Identify the parasite.
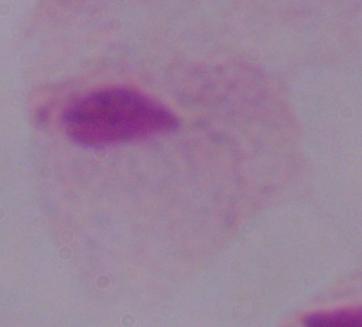
This is a trichomonad.

Captured at 1000x magnification. Photomicrograph.